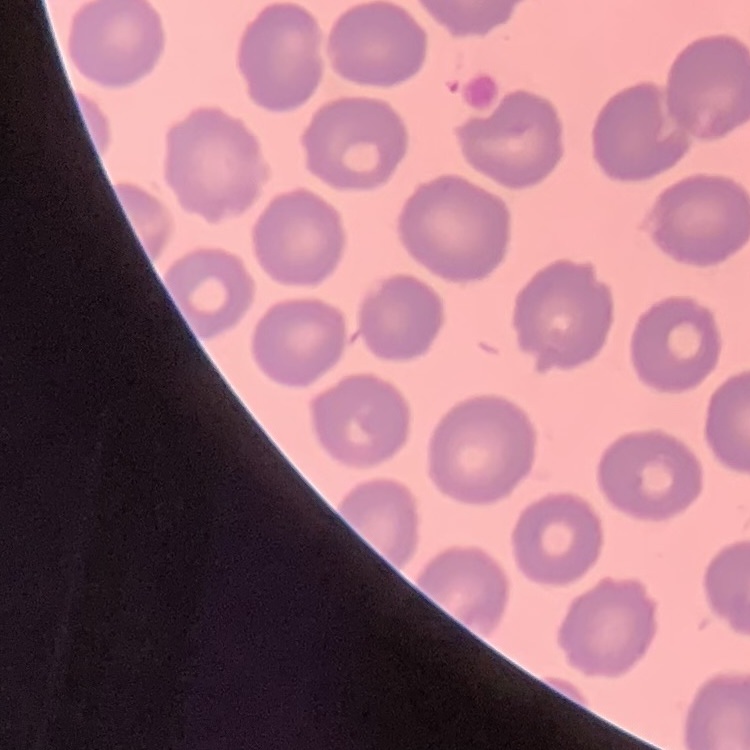

red blood cell morphology = no rouleaux formation
image type = square crop of a larger photomicrograph
stain = Field's or Giemsa
preparation = thin peripheral smear